Report the malaria status of this cell.
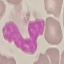
Uninfected.

Acquired by smartphone through the microscope eyepiece. Automatically extracted cell patch, resized to 64 × 64 pixels. Giemsa-stained preparation. Thin blood smear.